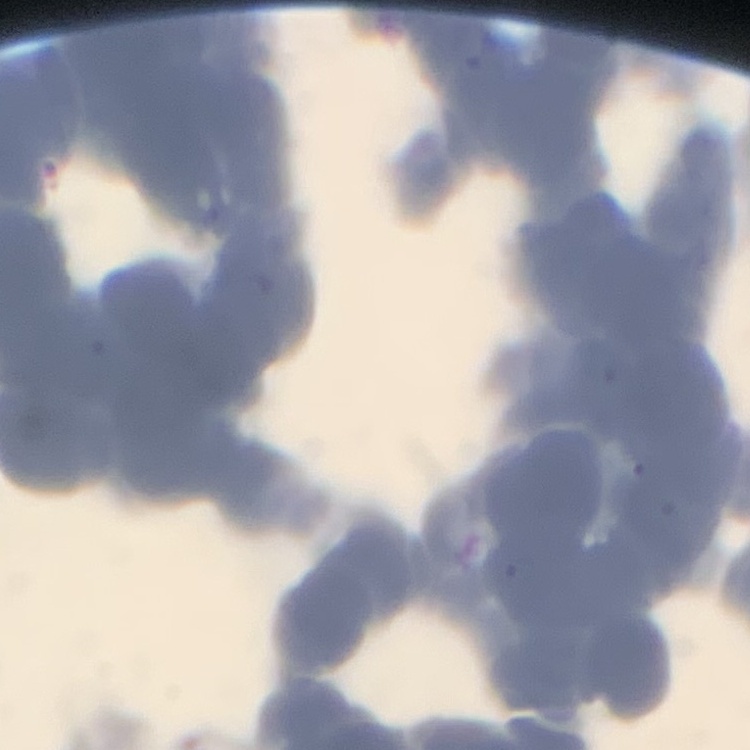
Summary:
  - Erythrocyte morphology: rouleaux formation
  - Stain: Field's or Giemsa
  - Image type: square crop of a larger photomicrograph
  - Preparation: thin blood film